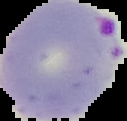

Result: malaria parasites detected. Cell region segmented out of the field of view; the surrounding area is masked to black. From a thin blood smear. Image is 127×121 pixels.